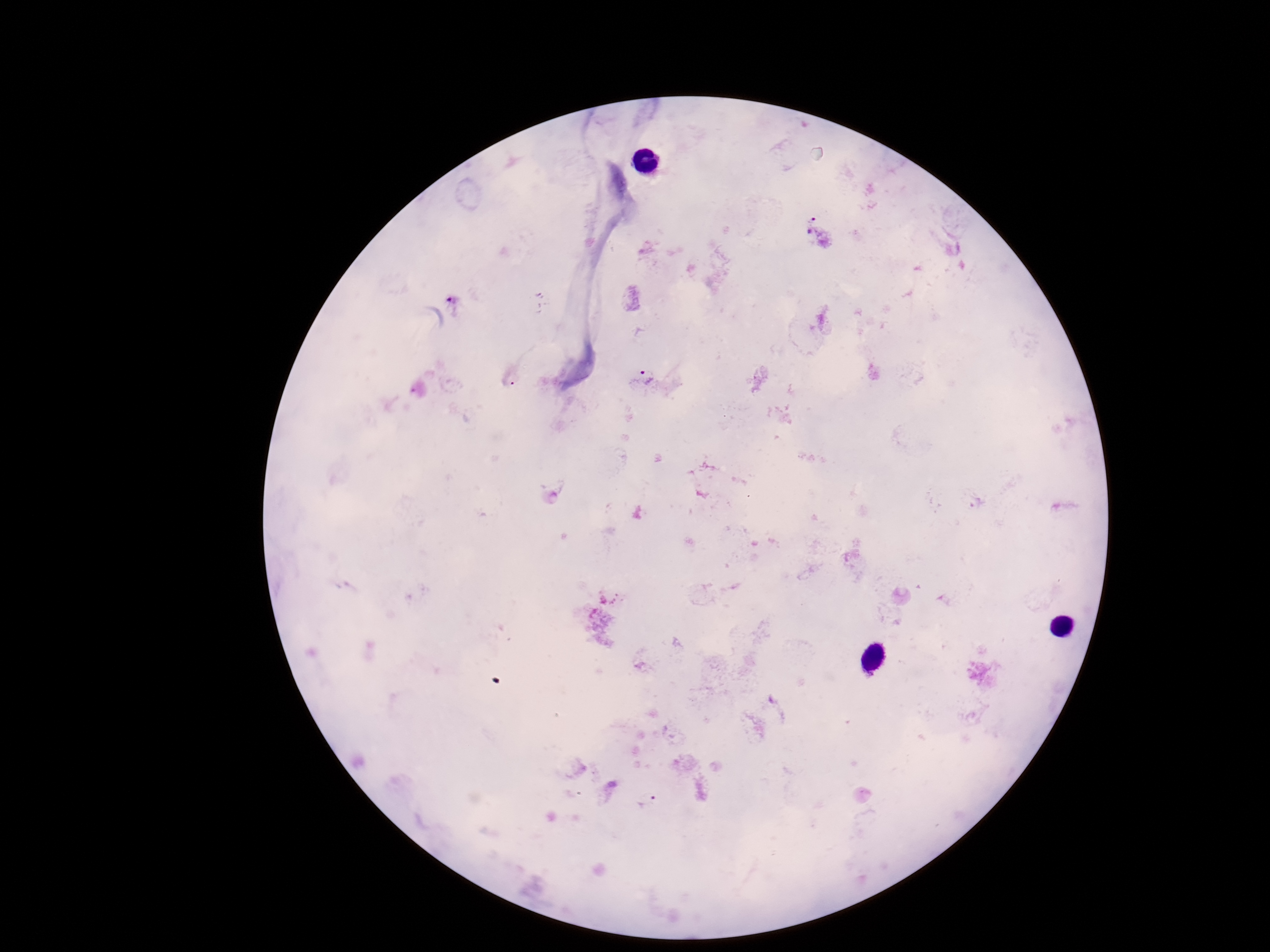
capture = smartphone camera through the microscope eyepiece
patient malaria status = positive
field of view = single
magnification = 100x
image size = 1270×952 pixels
stain = Giemsa
Plasmodium parasite locations = approximate centers as (x, y) in pixels: (818, 230), (648, 376), (510, 377), (647, 802)
preparation = thick blood smear